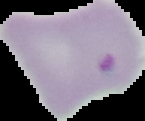
{
  "image_type": "cell region segmented out of the field of view; surrounding area masked to black",
  "image_size": "145×121 pixels",
  "preparation": "thin blood film",
  "malaria_status": "parasitized"
}